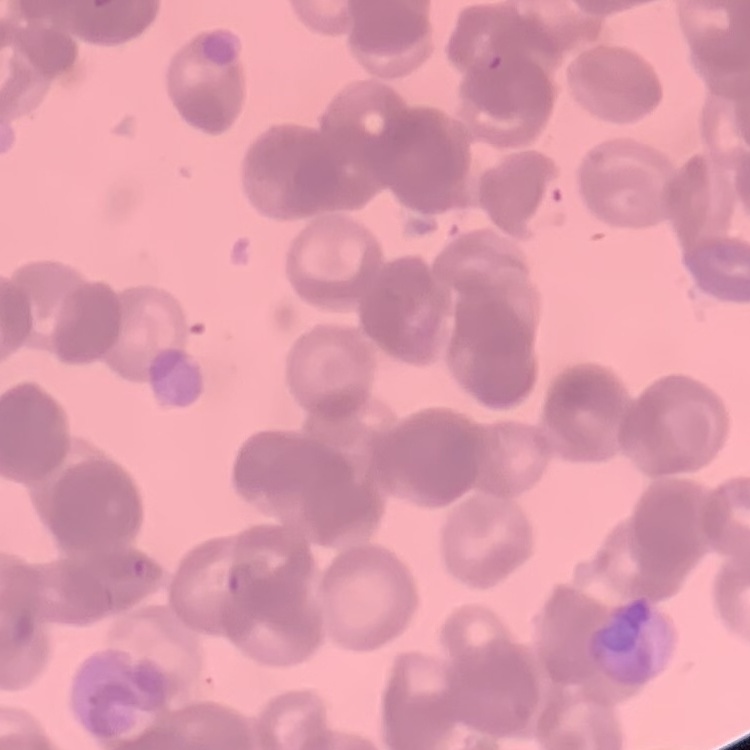
red blood cell morphology = rouleaux formation
preparation = thin blood film
image type = one tile cut from a larger photomicrograph
stain = Field's or Giemsa